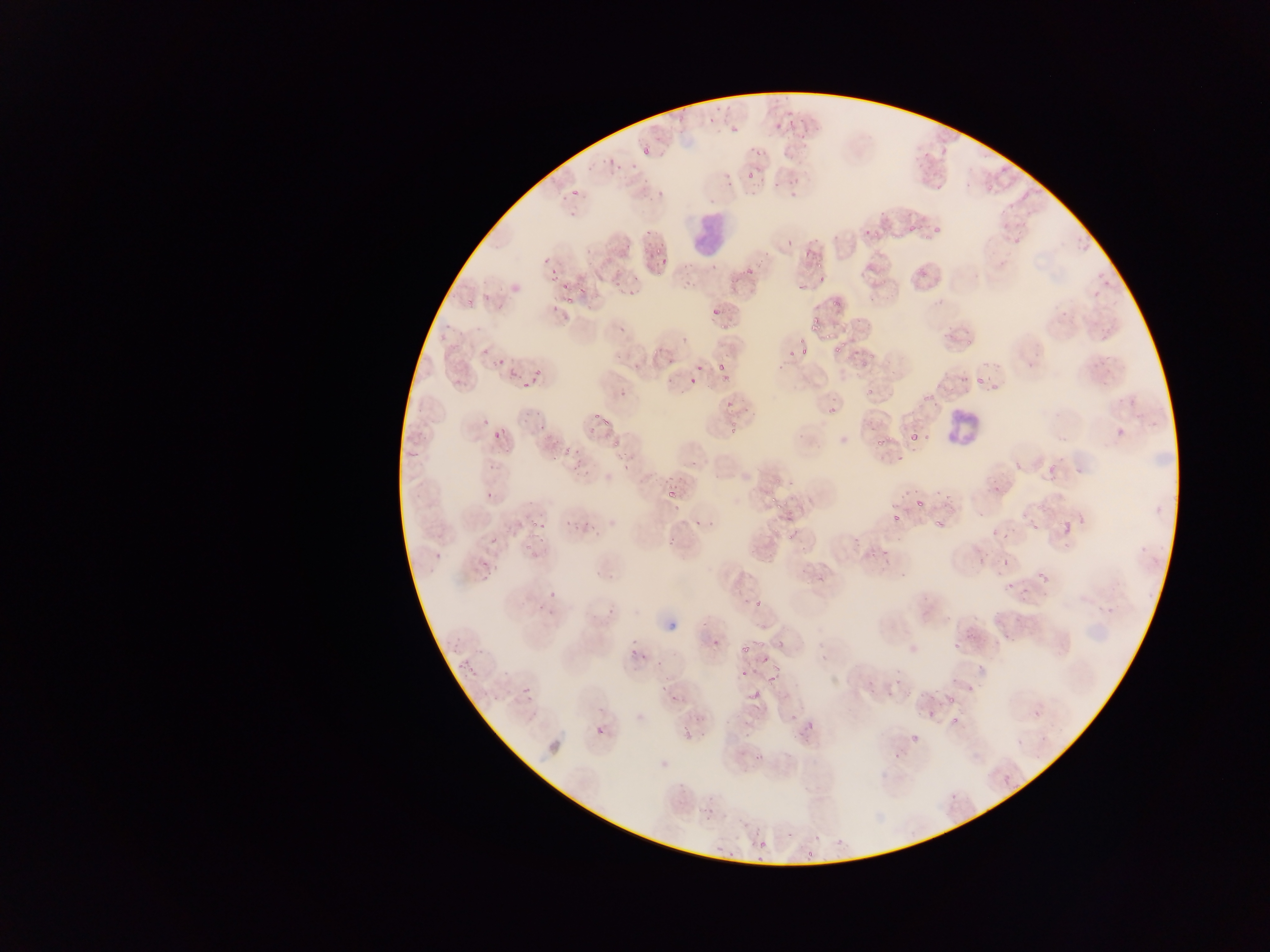

Approximate bounding boxes as (left, top, right, bottom) in pixels.
Summary:
  - Leukocyte locations: (685, 208, 732, 263), (941, 403, 986, 454)
  - Malaria parasite locations: (905, 220, 917, 235), (929, 222, 946, 236), (862, 230, 874, 238), (782, 239, 796, 251), (654, 248, 665, 254), (802, 251, 811, 261), (542, 254, 552, 268), (658, 261, 667, 269), (813, 266, 833, 284), (743, 269, 756, 275), (549, 271, 562, 283), (580, 274, 588, 297), (560, 286, 568, 292), (463, 292, 478, 308), (567, 292, 587, 304), (830, 295, 849, 310), (712, 310, 720, 314), (717, 319, 731, 330), (808, 319, 822, 333), (943, 327, 954, 342), (832, 334, 849, 354), (788, 336, 804, 364), (961, 336, 976, 350), (859, 345, 873, 367), (479, 346, 491, 358), (650, 347, 663, 362), (797, 348, 809, 359), (493, 354, 507, 369), (696, 365, 705, 373), (715, 365, 727, 370), (533, 367, 544, 379), (505, 369, 516, 385), (685, 371, 699, 385), (720, 372, 731, 382), (975, 374, 989, 387), (518, 376, 538, 393), (455, 377, 466, 390), (864, 387, 874, 397), (722, 401, 734, 417), (824, 402, 839, 416), (476, 406, 497, 428), (857, 409, 878, 430), (537, 418, 555, 437), (600, 418, 611, 428), (726, 418, 741, 433), (1115, 426, 1124, 435), (496, 427, 510, 437), (909, 432, 922, 443), (918, 433, 931, 442), (876, 435, 887, 447), (608, 437, 622, 459), (556, 441, 570, 460), (893, 449, 907, 464), (569, 456, 581, 474), (1008, 459, 1019, 470), (1048, 461, 1060, 471), (774, 466, 787, 483), (1048, 472, 1059, 482), (943, 483, 957, 499), (992, 483, 1004, 493), (667, 486, 678, 496), (482, 489, 495, 502), (934, 489, 942, 497), (768, 496, 783, 511), (915, 497, 929, 506), (669, 499, 684, 512), (1073, 505, 1086, 525), (891, 512, 903, 525), (563, 514, 574, 530), (580, 518, 597, 532), (927, 518, 944, 533), (1062, 518, 1075, 532), (528, 519, 544, 537), (1030, 519, 1041, 531), (773, 523, 781, 534), (1001, 530, 1009, 538), (786, 531, 797, 539), (894, 531, 904, 545), (488, 532, 505, 549), (668, 539, 676, 548), (520, 544, 530, 551), (877, 545, 890, 559), (527, 549, 540, 557), (976, 550, 990, 564), (433, 551, 445, 564), (1000, 554, 1013, 567), (479, 565, 496, 584), (1032, 568, 1053, 588), (1005, 578, 1017, 597), (546, 588, 559, 599), (753, 593, 764, 609), (534, 602, 543, 611), (1007, 631, 1015, 643), (712, 632, 723, 649), (953, 638, 962, 649), (754, 641, 765, 647), (740, 643, 751, 653), (629, 650, 639, 661), (640, 653, 648, 663), (755, 654, 776, 674), (462, 657, 484, 680), (739, 668, 751, 679), (764, 671, 779, 688), (895, 672, 909, 686), (658, 681, 669, 694), (522, 687, 535, 703), (751, 687, 764, 703), (903, 689, 912, 700), (947, 691, 958, 704), (669, 697, 680, 705), (927, 707, 938, 719), (951, 716, 962, 727), (805, 718, 817, 730), (908, 723, 923, 745), (595, 725, 607, 738), (1000, 772, 1016, 789), (757, 840, 768, 851), (716, 843, 726, 851), (800, 850, 820, 860) | approximate (x, y) pixel centers of objects too small to bound: (825, 339), (836, 843)
  - Country: Ghana
  - Image size: 1270×952 pixels
  - Field of view: single
  - Preparation: thin blood film
  - Capture: mobile-phone photograph through a microscope